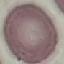

Result: no malaria parasites detected. Acquired by smartphone through the microscope eyepiece. Giemsa stain. Cell patch, automatically extracted from a larger field of view and resized to 64 × 64 pixels. Thin blood film.